Identify the blood parasite species.
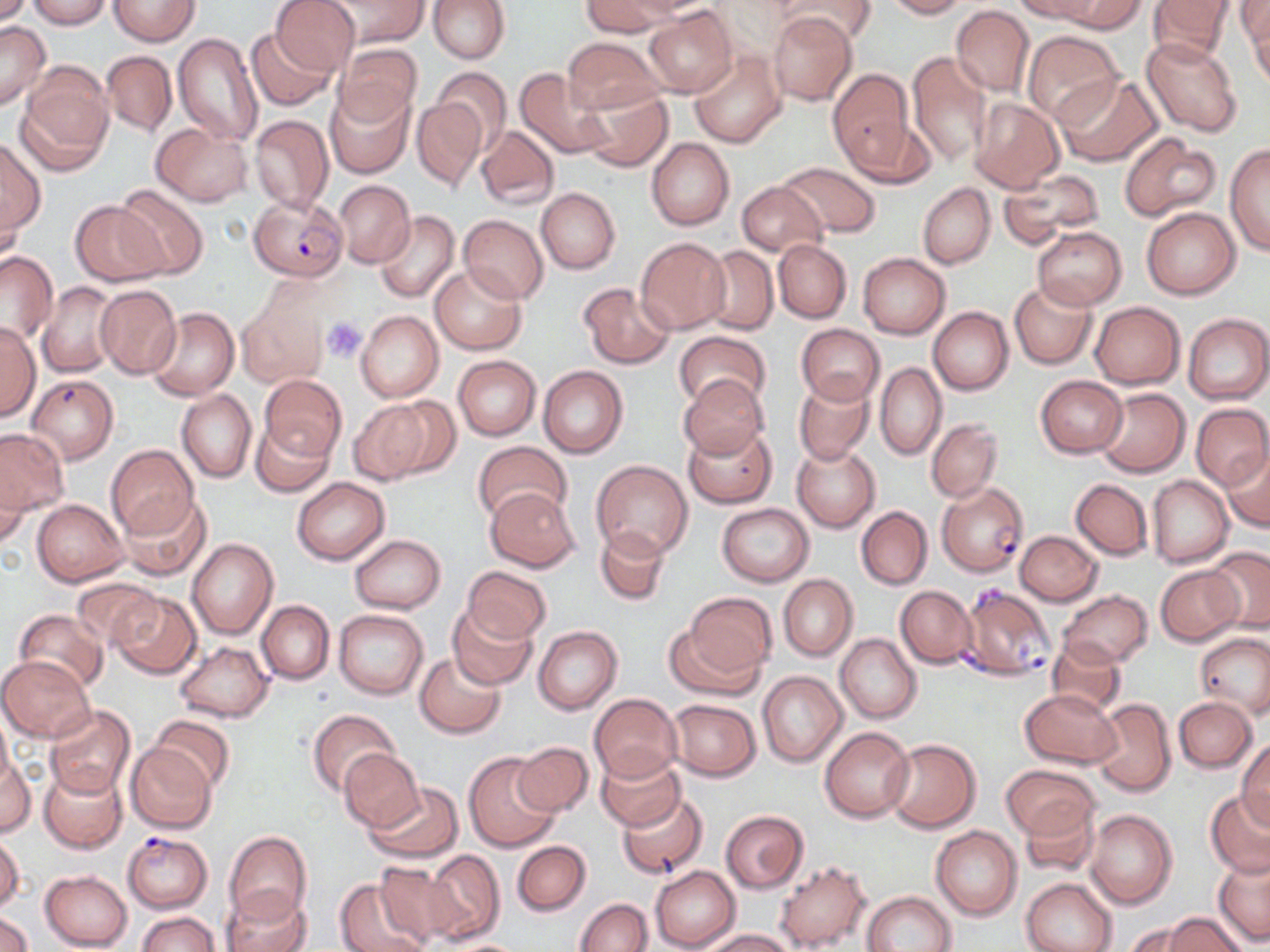

Plasmodium falciparum.

Approximate bounding boxes as (x1, y1, x2, y2) in pixels. Plasmodium falciparum-infected red blood cell locations: (248, 193, 347, 280), (26, 380, 113, 468), (937, 481, 1029, 577), (958, 583, 1056, 679), (121, 831, 213, 912). Uninfected red blood cell locations: (0, 0, 32, 27), (26, 0, 111, 29), (108, 0, 200, 46), (270, 0, 359, 74), (324, 0, 429, 49), (580, 0, 674, 37), (777, 0, 875, 47), (882, 0, 969, 19), (1011, 0, 1107, 23), (1049, 0, 1144, 33), (1147, 0, 1235, 66), (1240, 0, 1269, 70), (428, 1, 509, 63), (642, 6, 737, 97), (950, 6, 1034, 96), (768, 12, 858, 106), (0, 22, 49, 110), (246, 27, 337, 112), (1022, 30, 1125, 128), (172, 32, 264, 146), (1141, 37, 1244, 137), (563, 38, 663, 113), (334, 44, 422, 125), (690, 50, 786, 148), (101, 51, 175, 136), (907, 52, 995, 167), (20, 64, 113, 166), (517, 67, 614, 157), (433, 68, 512, 148), (828, 68, 918, 177), (1054, 74, 1160, 167), (324, 87, 414, 177), (578, 87, 673, 172), (412, 96, 487, 190), (970, 99, 1063, 193), (249, 114, 333, 215), (150, 122, 253, 206), (475, 125, 559, 210), (1118, 135, 1220, 220), (0, 137, 45, 239), (646, 138, 734, 231), (1226, 143, 1270, 257), (778, 162, 882, 239), (998, 170, 1104, 245), (333, 180, 416, 268), (737, 181, 828, 256), (918, 183, 995, 269), (115, 184, 209, 278), (535, 187, 620, 274), (70, 201, 166, 286), (1141, 207, 1240, 299), (374, 210, 460, 303), (459, 214, 549, 304), (1034, 227, 1126, 309), (636, 237, 730, 333), (773, 240, 852, 323), (701, 245, 778, 335), (0, 252, 58, 343), (858, 253, 951, 339), (430, 265, 526, 354), (1009, 280, 1097, 369), (38, 281, 121, 377), (578, 283, 674, 368), (94, 284, 181, 378), (1011, 292, 1180, 378), (237, 299, 327, 388), (1089, 301, 1185, 389), (148, 306, 238, 401), (929, 306, 1014, 395), (356, 310, 444, 402), (1182, 313, 1270, 405), (0, 322, 40, 421), (796, 323, 884, 405), (673, 331, 770, 410), (452, 355, 541, 441), (875, 364, 946, 460), (538, 366, 628, 457), (261, 374, 345, 460), (678, 375, 771, 459), (1035, 375, 1128, 458), (793, 376, 874, 465), (1094, 388, 1189, 478), (177, 390, 256, 483), (377, 396, 462, 481), (348, 400, 432, 484), (1191, 404, 1270, 491), (926, 418, 1002, 503), (251, 419, 334, 497), (682, 425, 776, 509), (0, 429, 70, 515), (472, 439, 571, 524), (791, 443, 880, 532), (105, 444, 199, 540), (1222, 444, 1270, 531), (0, 457, 29, 542), (591, 460, 695, 560), (1147, 475, 1234, 567), (292, 477, 389, 564), (1071, 479, 1153, 560), (486, 485, 581, 572), (117, 492, 214, 582), (32, 498, 128, 585), (716, 502, 815, 587), (856, 505, 932, 590), (594, 525, 671, 607), (1015, 530, 1102, 605), (349, 534, 445, 613), (186, 538, 278, 640), (1204, 546, 1270, 634), (461, 564, 551, 645), (1155, 564, 1244, 646), (779, 574, 858, 661), (72, 577, 161, 647), (896, 585, 978, 669), (1058, 590, 1153, 668), (110, 591, 201, 679), (686, 592, 777, 675), (256, 599, 335, 684), (447, 606, 537, 690), (14, 610, 108, 692), (334, 610, 428, 699), (665, 614, 768, 699), (533, 626, 622, 715), (1196, 632, 1270, 717), (836, 633, 921, 724), (1046, 638, 1126, 716), (176, 639, 273, 722), (414, 651, 506, 739), (0, 656, 94, 741), (757, 671, 847, 767), (1020, 689, 1121, 767), (590, 693, 683, 783), (1174, 696, 1257, 772), (1090, 698, 1175, 797), (665, 699, 762, 781), (44, 705, 138, 800), (307, 709, 401, 797), (0, 710, 14, 794), (150, 715, 236, 792), (820, 726, 915, 822), (883, 738, 980, 833), (1235, 740, 1270, 828), (512, 741, 593, 816), (125, 743, 215, 833), (340, 751, 423, 831), (463, 752, 563, 852), (595, 753, 684, 832), (0, 755, 37, 838), (1001, 764, 1100, 840), (38, 766, 127, 854), (362, 781, 464, 863), (1205, 789, 1270, 879), (616, 791, 708, 880), (1019, 799, 1101, 878), (1085, 809, 1177, 910), (721, 810, 809, 894), (930, 825, 1022, 921), (225, 830, 312, 920), (1, 834, 23, 913), (511, 841, 591, 916), (424, 850, 505, 943), (1212, 854, 1270, 947), (375, 859, 469, 946), (775, 860, 870, 951), (651, 866, 741, 951), (40, 869, 133, 950), (333, 876, 434, 952), (1022, 877, 1117, 952), (222, 886, 312, 952), (863, 891, 957, 952), (576, 898, 652, 951), (0, 909, 35, 952), (137, 911, 221, 952), (1162, 913, 1247, 952), (1121, 921, 1210, 952), (703, 929, 797, 951). Platelet locations: (323, 317, 366, 359). Image is 1270×952 pixels. Light microscopy. Single field of view. May-Grünwald-Giemsa-stained preparation. 1000x magnification. Thin blood film.